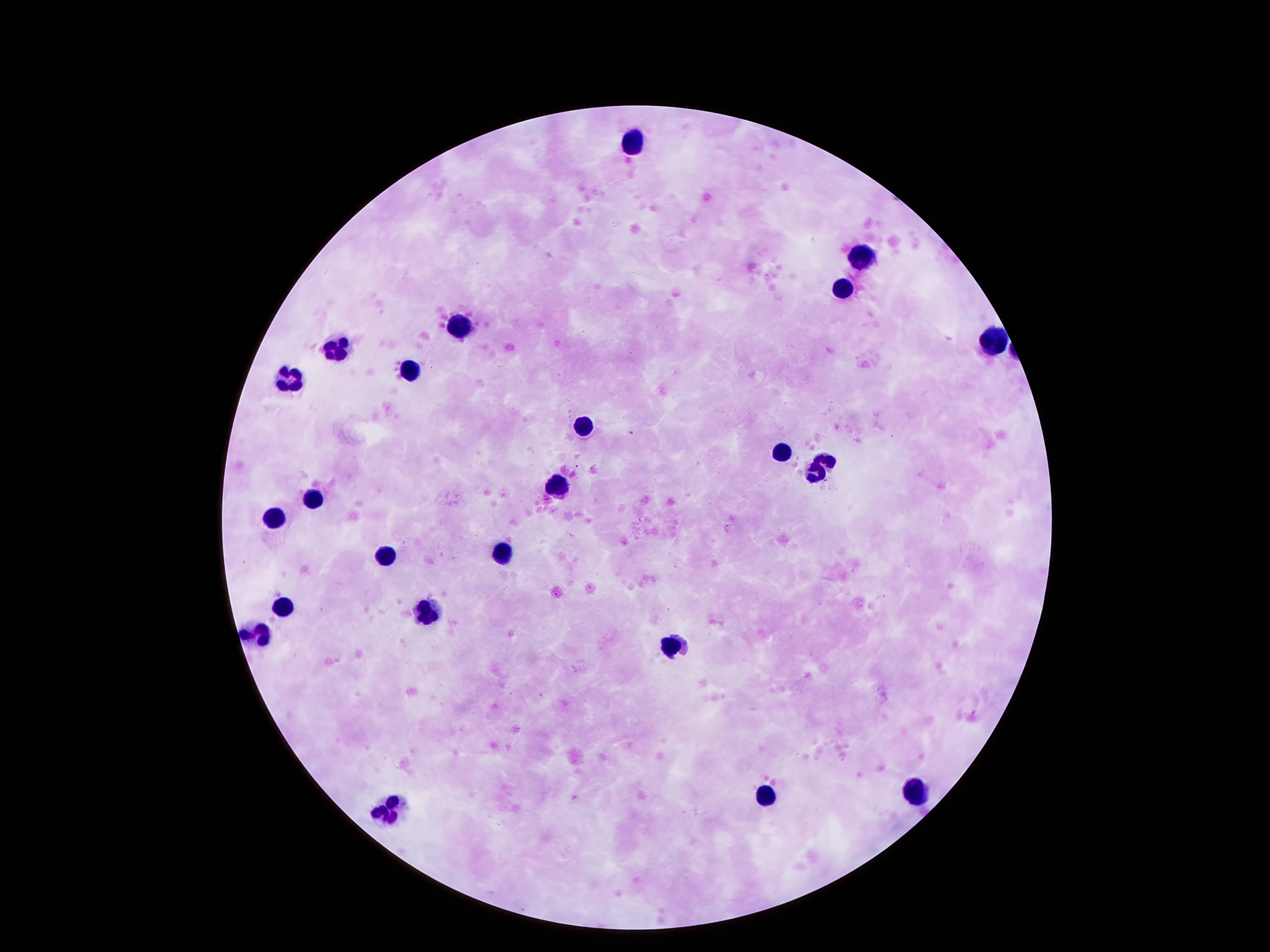

{
  "leukocyte_locations": "approximate object centers, in pixels from the top-left corner: (x=629, y=145), (x=869, y=253), (x=845, y=287), (x=459, y=324), (x=995, y=341), (x=335, y=350), (x=414, y=370), (x=283, y=381), (x=587, y=430), (x=784, y=452), (x=829, y=455), (x=813, y=473), (x=556, y=480), (x=311, y=497), (x=272, y=519), (x=382, y=552), (x=503, y=552), (x=285, y=604), (x=427, y=611), (x=254, y=631), (x=671, y=648), (x=913, y=790), (x=763, y=796), (x=390, y=809)",
  "magnification": "100x",
  "preparation": "thick peripheral-blood smear",
  "field_of_view": "single",
  "stain": "Giemsa",
  "image_size": "1270×952 pixels",
  "capture": "smartphone camera through the microscope eyepiece",
  "patient_malaria_status": "not infected"
}